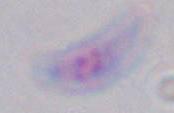

modality = micrograph
magnification = 1000x
identification = Toxoplasma gondii